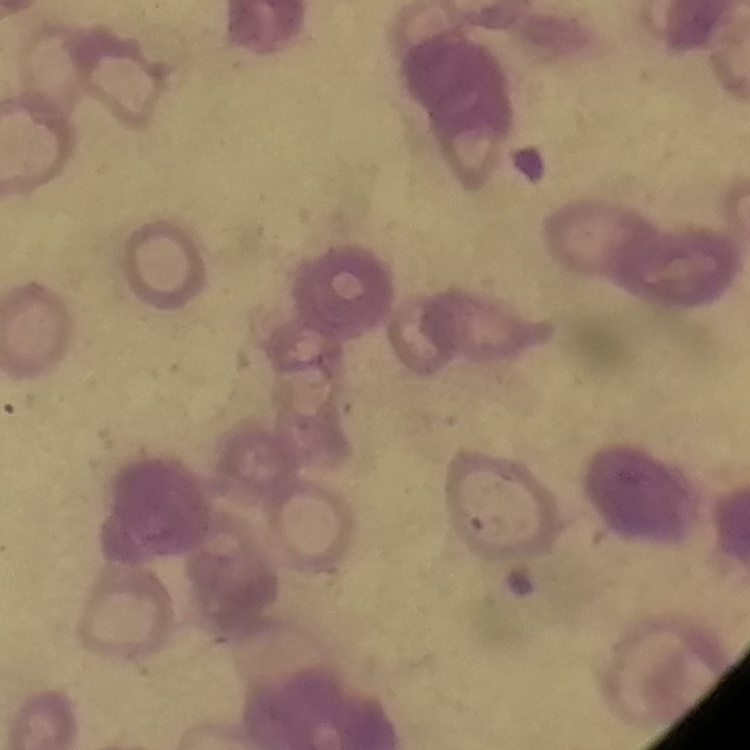
Summary:
  - Erythrocyte morphology: rouleaux formation
  - Preparation: thin blood smear
  - Image type: square crop of a larger photomicrograph
  - Stain: Field's or Giemsa